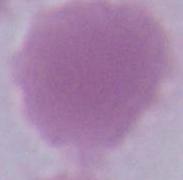
Summary:
  - Identification: red blood cell
  - Magnification: 1000x
  - Modality: photomicrograph